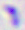
magnification: 400x
modality: photomicrograph
identification: Toxoplasma gondii